Describe the morphology of the red blood cells.
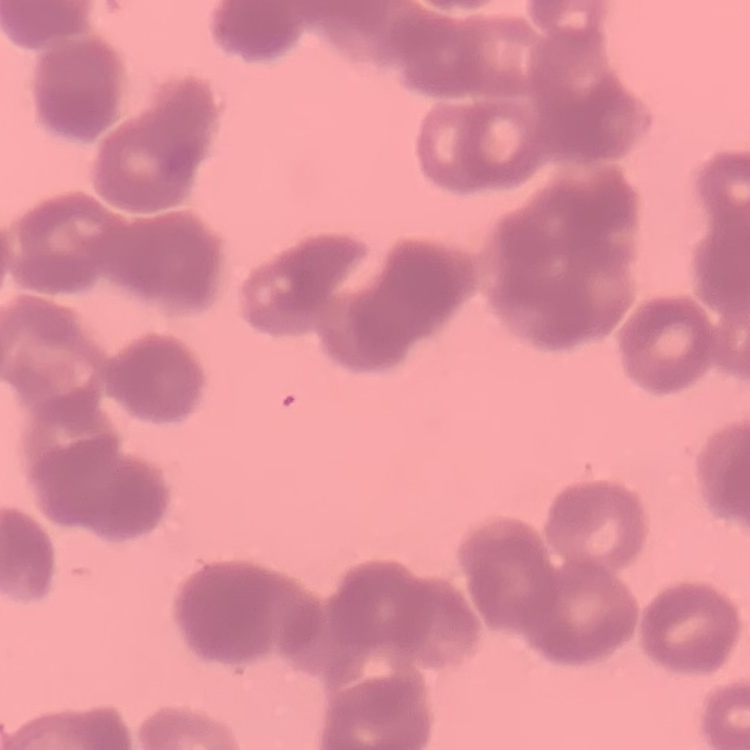
They show rouleaux formation.

stain = Field's or Giemsa
preparation = thin blood smear
image type = square crop of a larger photomicrograph